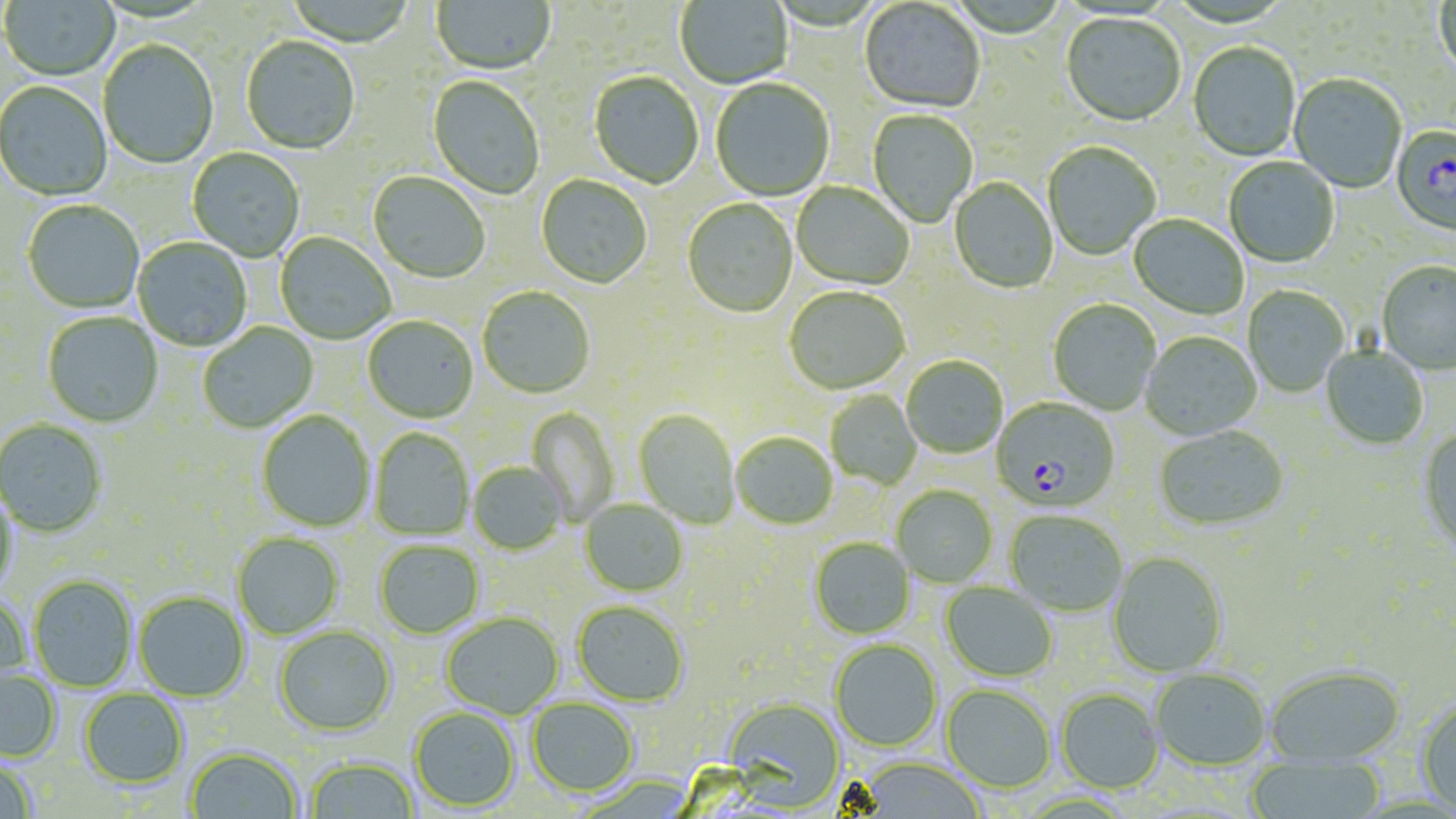

Approximate bounding boxes as [x1, y1, x2, y2] in pixels. Plasmodium falciparum-infected red blood cell locations: [1391, 126, 1456, 239], [991, 398, 1120, 512]. Uninfected red blood cell locations: [1, 0, 120, 82], [286, 0, 416, 49], [431, 0, 555, 77], [673, 0, 794, 90], [859, 1, 984, 115], [1435, 1, 1456, 81], [1061, 14, 1186, 129], [241, 37, 359, 155], [98, 41, 219, 170], [1188, 44, 1300, 162], [589, 73, 704, 190], [1289, 75, 1406, 194], [427, 76, 545, 200], [710, 79, 835, 202], [0, 82, 112, 201], [867, 110, 978, 228], [1043, 143, 1161, 261], [187, 148, 305, 262], [1224, 157, 1340, 269], [368, 172, 490, 284], [536, 175, 652, 290], [949, 178, 1058, 294], [792, 183, 913, 291], [22, 200, 145, 314], [682, 200, 798, 319], [1128, 215, 1249, 320], [275, 232, 395, 344], [133, 237, 252, 352], [1377, 263, 1456, 376], [1242, 286, 1349, 397], [477, 287, 595, 399], [785, 288, 910, 396], [1048, 300, 1161, 416], [42, 311, 163, 428], [363, 316, 479, 423], [198, 322, 318, 434], [1141, 332, 1262, 441], [1320, 347, 1429, 451], [901, 356, 1008, 459], [825, 390, 922, 489], [526, 407, 619, 525], [634, 410, 741, 529], [256, 411, 375, 532], [0, 420, 107, 537], [370, 428, 474, 541], [1154, 428, 1289, 533], [1417, 429, 1456, 557], [732, 433, 837, 530], [468, 462, 568, 556], [0, 485, 20, 599], [892, 486, 998, 587], [580, 500, 688, 597], [1005, 511, 1127, 617], [232, 532, 343, 639], [809, 538, 915, 639], [375, 541, 484, 639], [1108, 552, 1229, 679], [28, 574, 138, 692], [940, 582, 1057, 682], [134, 591, 250, 702], [0, 594, 31, 690], [572, 602, 689, 707], [441, 613, 564, 719], [274, 626, 397, 736], [830, 640, 942, 751], [1265, 666, 1405, 768], [0, 669, 61, 762], [1151, 669, 1270, 771], [942, 685, 1055, 793], [79, 688, 188, 788], [1056, 688, 1165, 794], [724, 697, 846, 811], [527, 698, 639, 797], [1415, 698, 1456, 815], [409, 707, 520, 812], [185, 748, 302, 819], [305, 756, 420, 819], [1245, 757, 1386, 819], [855, 758, 985, 818], [0, 759, 37, 819]. Slide-level diagnosis: Plasmodium falciparum. Single field of view. May-Grünwald-Giemsa-stained preparation. Image is 1456×819 pixels. Captured at 1000x magnification. Optical microscopy. Thin blood smear.